Draw a bounding box around every parasitised red blood cell.
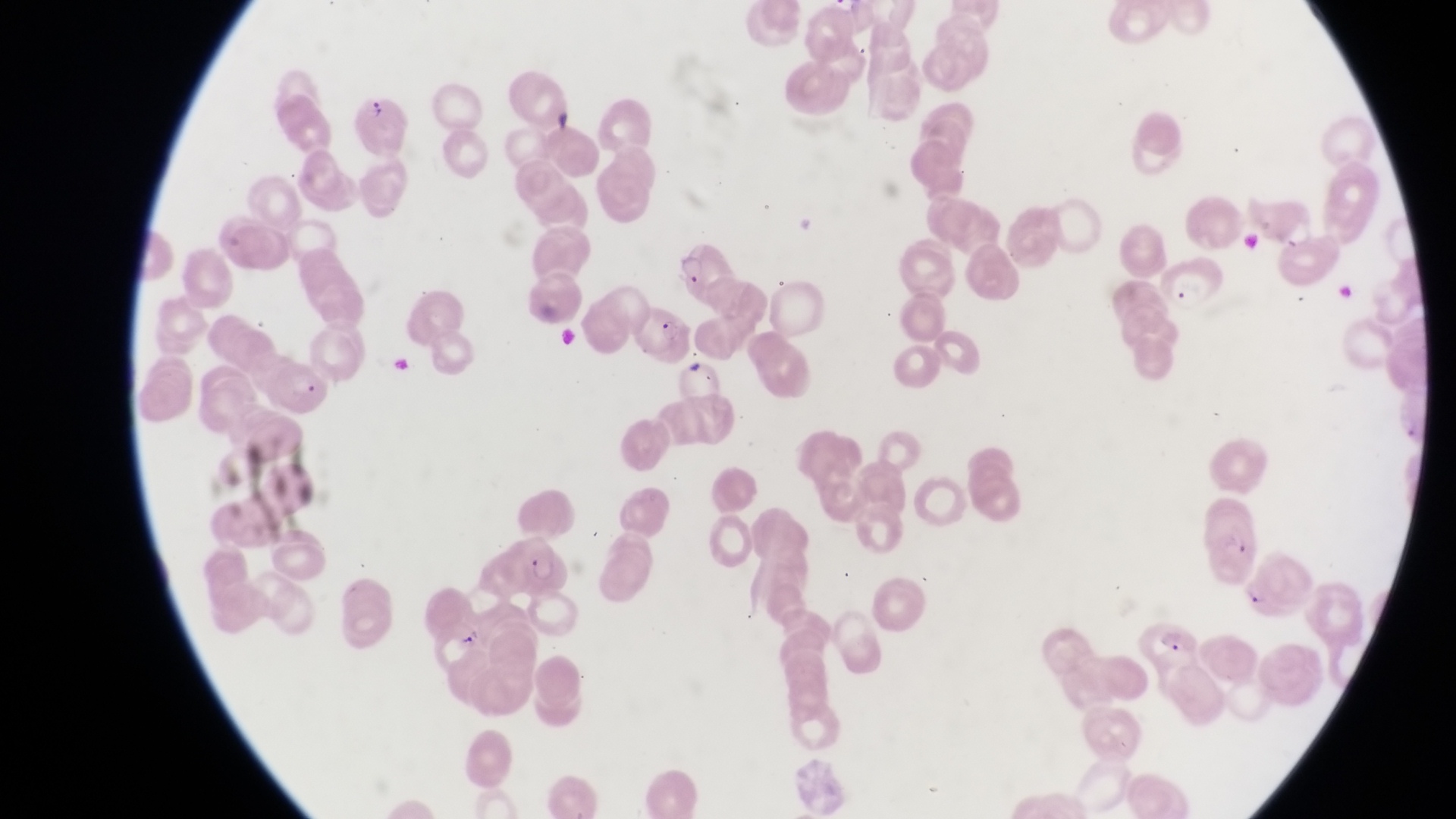
Approximate bounding boxes as (left, top, right, bottom) in pixels.
Parasitised red blood cells: (357, 95, 413, 155), (667, 241, 723, 297), (1156, 258, 1225, 321), (635, 307, 691, 365), (267, 360, 334, 419), (508, 532, 571, 596), (1144, 614, 1208, 664).

preparation = thin blood smear
field of view = single
image size = 1456×819 pixels
capture = smartphone photograph through the eyepiece of an Olympus CX-23 microscope
country = Uganda
magnification = 1000x